Locate and identify every blood parasite.
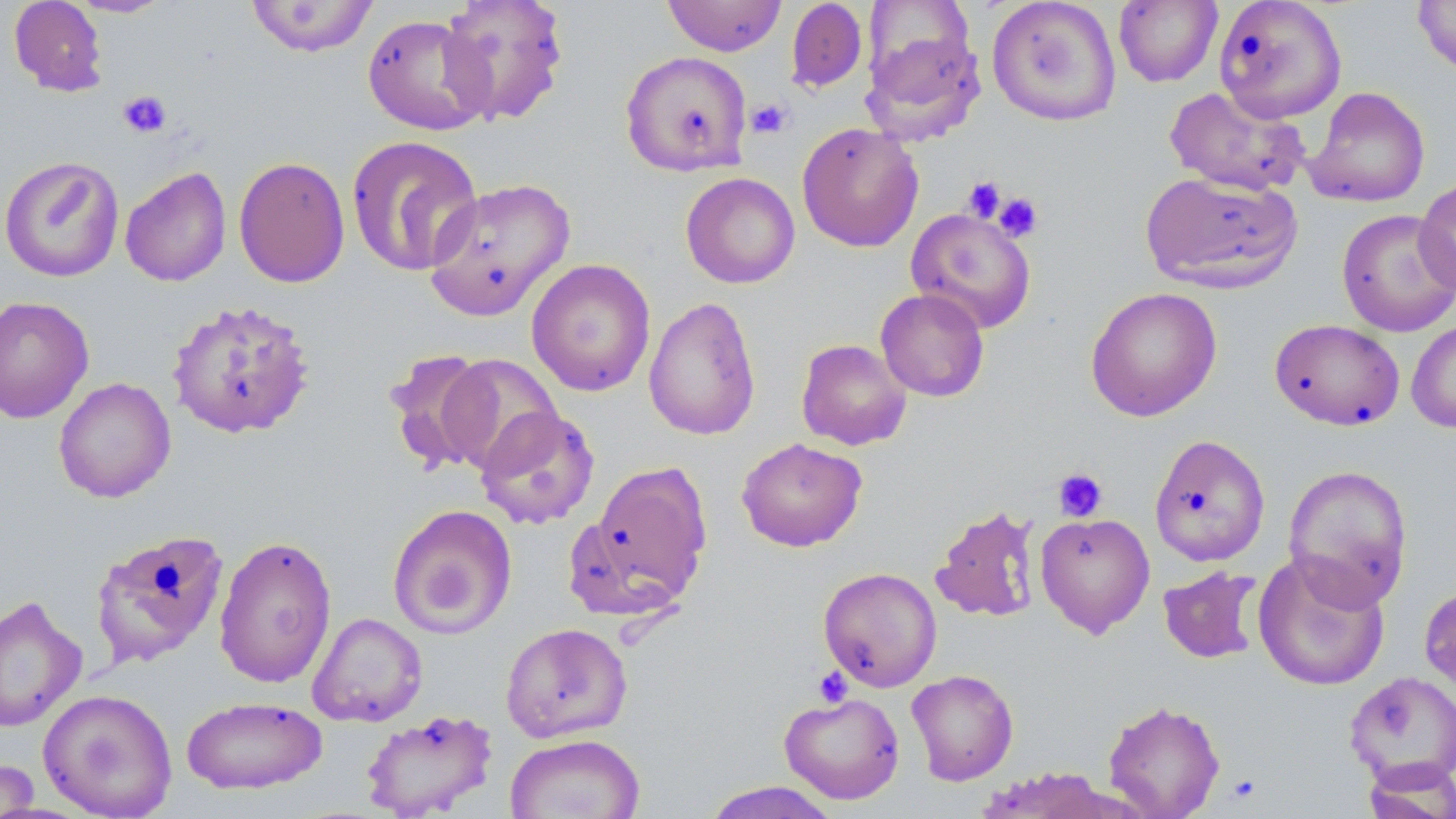
No blood parasites observed.

Approximate bounding boxes as [x1, y1, x2, y2] in pixels. Uninfected red blood cell locations: [8, 0, 108, 96], [66, 0, 175, 18], [438, 0, 570, 126], [662, 0, 787, 57], [786, 0, 868, 93], [987, 0, 1122, 126], [1113, 0, 1223, 88], [1213, 0, 1347, 123], [1412, 0, 1456, 77], [244, 1, 380, 57], [362, 13, 493, 136], [860, 26, 986, 145], [620, 50, 753, 176], [1164, 86, 1311, 197], [1305, 86, 1430, 208], [796, 122, 924, 252], [346, 135, 484, 277], [0, 155, 125, 283], [233, 156, 351, 288], [119, 166, 232, 287], [1140, 170, 1304, 294], [680, 172, 800, 288], [423, 177, 577, 321], [1414, 177, 1456, 297], [905, 207, 1037, 334], [1336, 209, 1456, 337], [526, 258, 656, 397], [1085, 286, 1223, 422], [875, 288, 990, 402], [0, 295, 95, 423], [643, 296, 762, 441], [165, 298, 316, 440], [1269, 318, 1405, 430], [1407, 320, 1456, 433], [796, 338, 911, 451], [383, 349, 496, 473], [437, 354, 564, 475], [53, 377, 177, 503], [475, 405, 600, 529], [1149, 434, 1271, 566], [736, 437, 868, 552], [585, 460, 712, 610], [1283, 464, 1414, 608], [387, 504, 518, 639], [930, 504, 1041, 622], [1035, 513, 1155, 637], [89, 528, 230, 670], [213, 534, 338, 689], [1252, 551, 1391, 692], [1158, 565, 1264, 665], [818, 567, 942, 692], [1419, 582, 1456, 706], [0, 594, 87, 733], [307, 612, 428, 727], [500, 622, 633, 743], [906, 669, 1019, 786], [1343, 670, 1456, 787], [38, 688, 178, 818], [779, 691, 905, 804], [181, 696, 327, 795], [1103, 699, 1225, 818], [360, 709, 498, 819], [505, 733, 646, 819], [1361, 758, 1456, 819], [0, 759, 40, 817], [700, 781, 842, 819]. Platelet locations: [118, 90, 172, 139], [745, 99, 793, 139], [962, 177, 1005, 222], [992, 192, 1044, 242], [1053, 467, 1108, 522], [813, 666, 853, 707], [1225, 773, 1261, 804]. Slide-level diagnosis: no evidence of blood parasites. Image is 1456×819 pixels. Single field of view. May-Grünwald-Giemsa-stained preparation. Thin blood smear. Light microscopy. 1000x magnification.